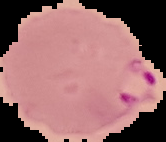
image size = 166×142 pixels
preparation = thin blood smear
image type = segmented cell region on a black background
result = Plasmodium parasites identified